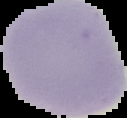 Malaria status: uninfected. Segmented cell region on a black background. From a thin blood film. Image is 127×118 pixels.